Point out each Plasmodium parasite.
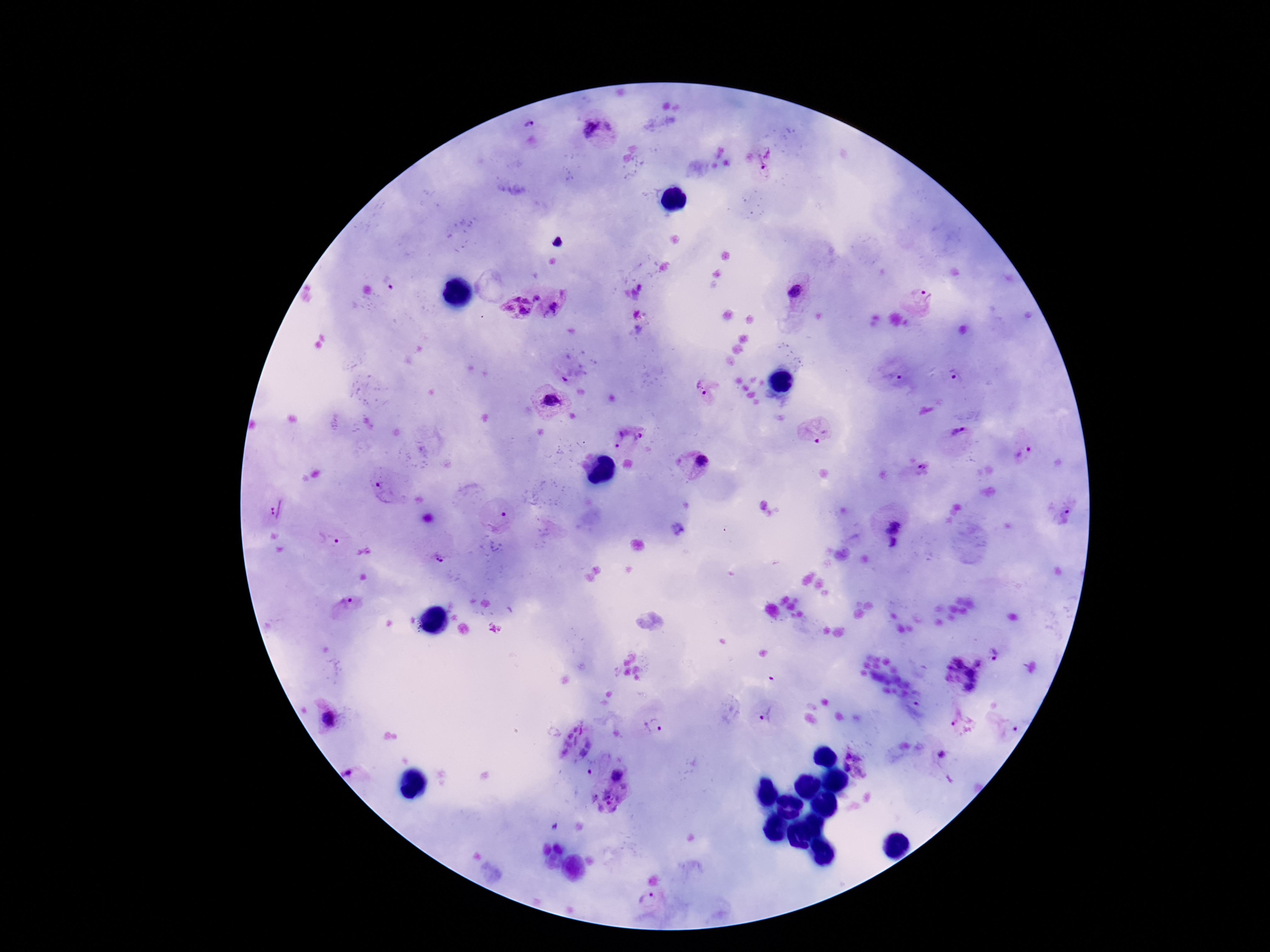
Approximate centers as [x, y] in pixels.
Plasmodium parasites: [529, 125], [609, 127], [590, 128], [767, 158], [796, 292], [537, 296], [923, 297], [514, 298], [526, 300], [508, 309], [554, 309], [525, 313], [893, 377], [955, 377], [573, 378], [702, 389], [551, 401], [814, 433], [959, 434], [616, 438], [639, 438], [1022, 455], [701, 463], [923, 467], [389, 490], [276, 508], [1067, 517], [501, 522], [894, 524], [891, 532], [330, 541], [893, 543], [439, 560], [343, 606], [995, 654], [979, 662], [954, 678], [767, 714], [328, 720], [962, 725], [653, 726], [574, 728], [583, 731], [568, 735], [578, 741], [589, 743], [568, 744], [565, 752], [582, 754], [942, 754], [856, 765], [351, 771], [589, 773], [616, 775], [647, 900].

Patient malaria status: infected. Thick blood smear. Smartphone photograph taken through the microscope eyepiece. Image is 1270×952 pixels. Single field of view. Giemsa stain. 100x magnification.